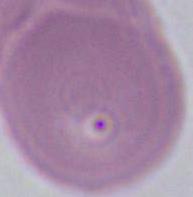

{
  "modality": "micrograph",
  "magnification": "1000x",
  "identification": "red blood cell"
}